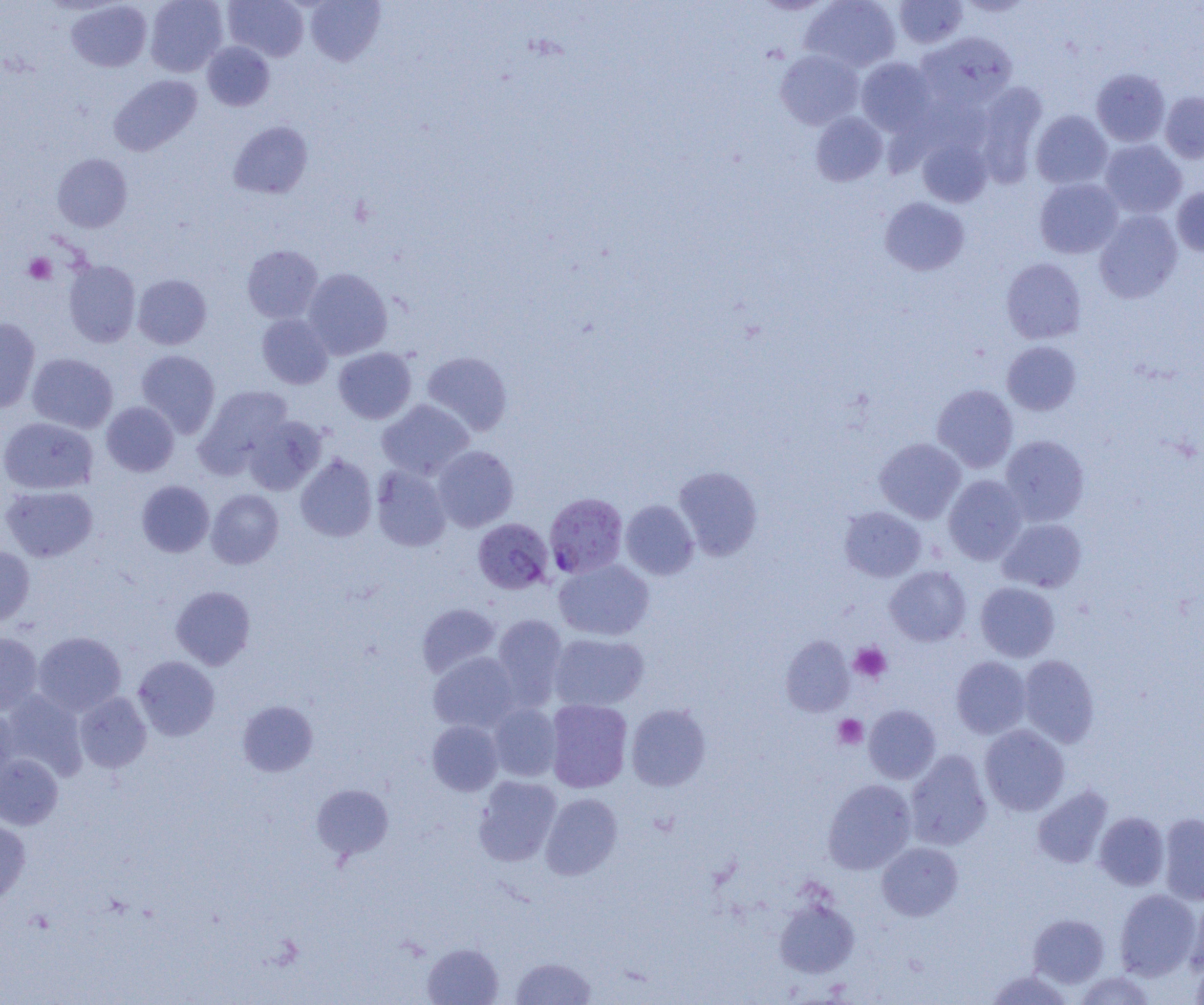

Summary:
  - Coordinate format: approximate bounding boxes as (x1, y1, x2, y2) in pixels
  - Uninfected red blood cell locations: (145, 0, 228, 76), (224, 0, 309, 61), (305, 0, 386, 66), (801, 0, 901, 73), (66, 1, 152, 72), (893, 1, 968, 48), (917, 32, 1018, 110), (202, 42, 274, 111), (775, 50, 863, 129), (856, 57, 936, 135), (1091, 68, 1170, 146), (109, 74, 202, 155), (974, 82, 1048, 187), (1160, 91, 1204, 163), (1031, 110, 1112, 189), (810, 112, 887, 186), (228, 121, 313, 199), (918, 138, 992, 207), (1099, 140, 1186, 218), (52, 154, 132, 232), (1034, 178, 1123, 258), (1171, 186, 1204, 256), (880, 197, 969, 275), (1094, 209, 1182, 303), (242, 245, 323, 323), (1001, 258, 1086, 343), (63, 259, 141, 347), (303, 268, 392, 359), (133, 273, 212, 349), (257, 314, 333, 389), (0, 318, 40, 413), (1002, 341, 1082, 415), (334, 347, 416, 424), (136, 349, 220, 437), (422, 351, 512, 436), (27, 352, 118, 433), (932, 383, 1018, 473), (195, 385, 293, 475), (377, 399, 474, 480), (101, 402, 179, 476), (243, 415, 326, 495), (0, 417, 98, 494), (1000, 435, 1089, 526), (875, 438, 966, 523), (432, 445, 518, 532), (295, 454, 377, 541), (371, 465, 451, 551), (674, 465, 763, 560), (943, 475, 1027, 564), (136, 480, 214, 557), (1, 485, 98, 562), (206, 489, 284, 568), (621, 500, 698, 580), (839, 506, 926, 582), (998, 518, 1086, 592), (0, 546, 35, 625), (553, 559, 654, 641), (884, 566, 972, 646), (975, 582, 1060, 661), (171, 586, 255, 670), (417, 603, 501, 678), (492, 614, 568, 705), (0, 632, 43, 715), (33, 632, 126, 716), (549, 633, 649, 711), (781, 636, 854, 716), (429, 652, 520, 732), (1018, 655, 1099, 747), (133, 656, 220, 741), (951, 656, 1031, 738), (1, 690, 87, 780), (74, 692, 152, 772), (545, 699, 632, 792), (238, 700, 318, 776), (626, 703, 711, 791), (488, 704, 561, 781), (863, 705, 941, 784), (0, 707, 17, 788), (427, 720, 503, 796), (979, 724, 1070, 816), (905, 750, 992, 851), (0, 753, 63, 829), (473, 776, 561, 865), (822, 779, 916, 874), (312, 783, 394, 859), (1032, 784, 1114, 869), (540, 793, 622, 880), (1094, 812, 1169, 890), (1158, 812, 1204, 905), (0, 818, 31, 903), (877, 841, 963, 920), (1114, 889, 1200, 980), (1185, 894, 1204, 977), (774, 897, 860, 979), (1029, 913, 1110, 987), (422, 942, 503, 1004), (1190, 952, 1204, 1005), (511, 957, 596, 1004), (986, 968, 1074, 1004), (1075, 971, 1157, 1005)
  - Plasmodium falciparum-infected red blood cell locations: (545, 493, 627, 578), (473, 518, 553, 594)
  - Platelet locations: (24, 253, 57, 284), (850, 642, 891, 682), (833, 714, 868, 749)
  - Slide-level diagnosis: Plasmodium falciparum
  - Field of view: single
  - Image size: 1204×1005 pixels
  - Magnification: 1000x
  - Preparation: thin blood smear
  - Modality: light microscopy